Locate every malaria parasite.
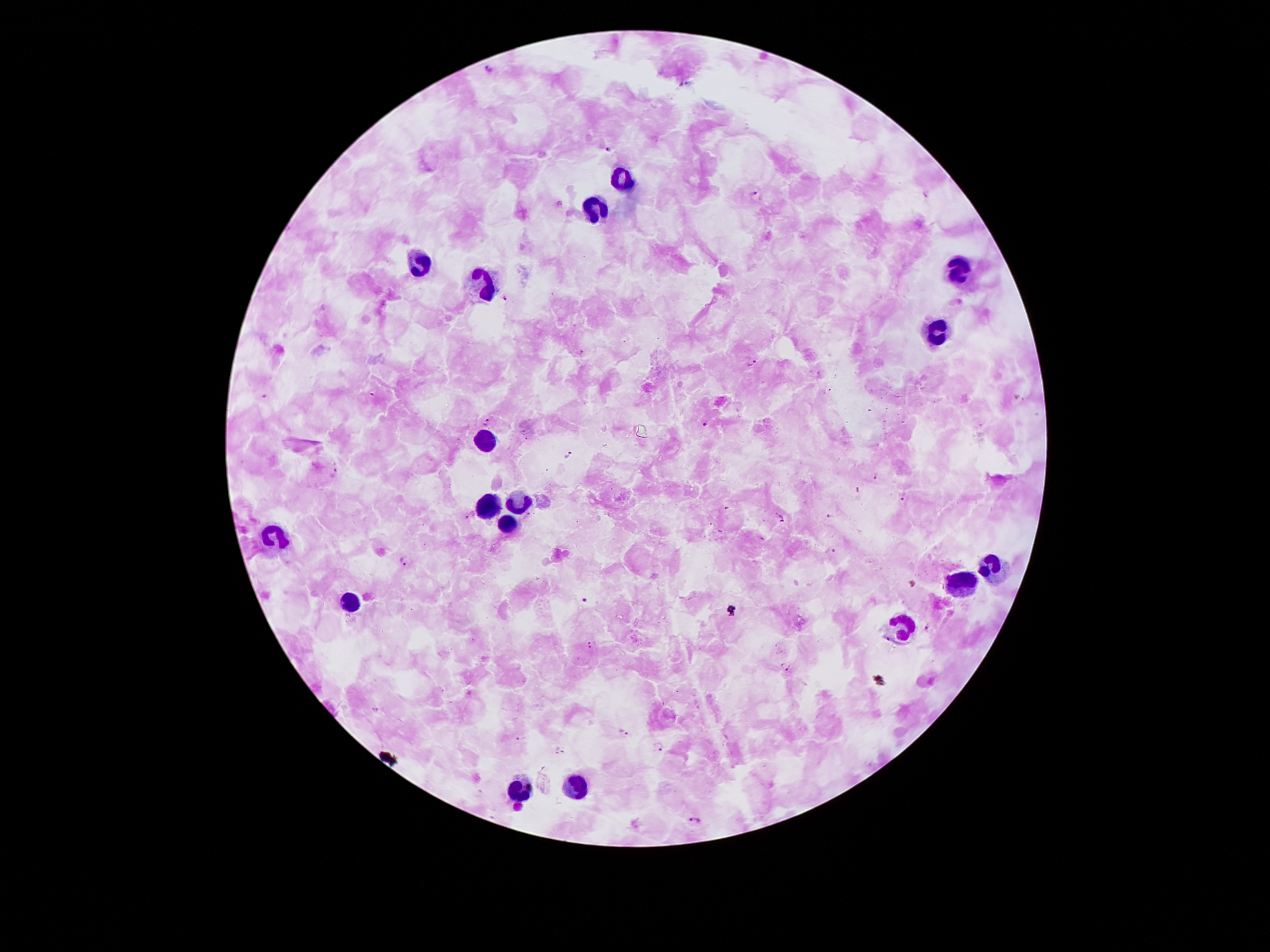

Approximate centers as [x, y] in pixels.
Malaria parasites: [488, 69], [609, 148], [757, 191], [504, 299], [753, 361], [485, 421], [707, 424], [567, 455], [333, 475], [875, 475], [858, 491], [902, 497], [725, 507], [529, 515], [830, 515], [781, 518], [834, 551], [404, 562], [913, 583], [586, 599], [926, 628], [590, 644], [788, 669], [622, 733], [659, 746], [561, 751], [694, 820].

Summary:
  - Leukocyte locations: [619, 175], [596, 205], [416, 265], [958, 267], [480, 283], [935, 335], [489, 444], [518, 499], [489, 505], [506, 525], [274, 538], [996, 563], [967, 576], [353, 601], [900, 631], [573, 784], [515, 790]
  - Stain: Giemsa
  - Preparation: thick blood smear
  - Magnification: 100x
  - Capture: smartphone camera through the microscope eyepiece
  - Field of view: one from this slide
  - Patient malaria status: positive for Plasmodium falciparum
  - Image size: 1270×952 pixels